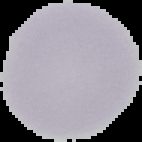
image type = cell region segmented out of the field of view; surrounding area masked to black
result = no Plasmodium parasites seen
preparation = thin blood film
image size = 142×142 pixels